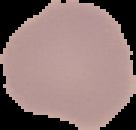
Summary:
  - Preparation: thin blood film
  - Image size: 136×130 pixels
  - Malaria status: uninfected
  - Image type: segmented cell region with the area outside set to black